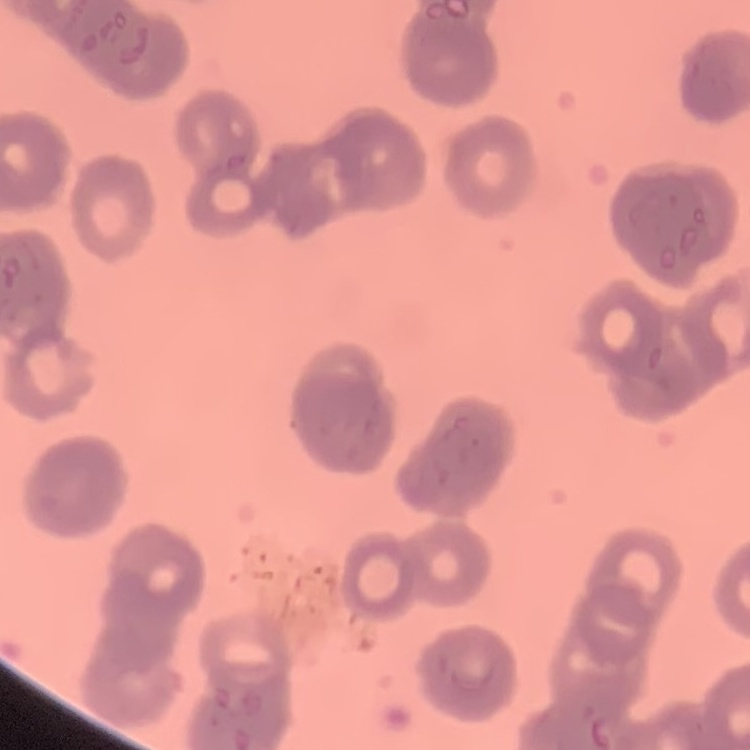 The erythrocytes exhibit rouleaux formation. Thin blood film. Square crop of a larger photomicrograph. Field's or Giemsa stain.